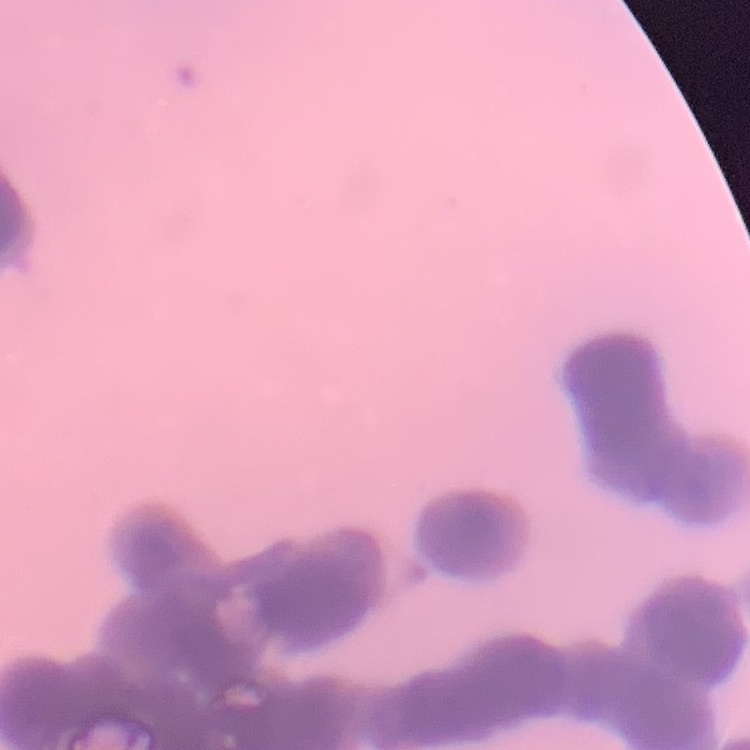
Summary:
  - Red blood cell morphology: rouleaux formation
  - Image type: one tile cut from a larger photomicrograph
  - Stain: Field's or Giemsa
  - Preparation: thin blood smear